Point out each leukocyte.
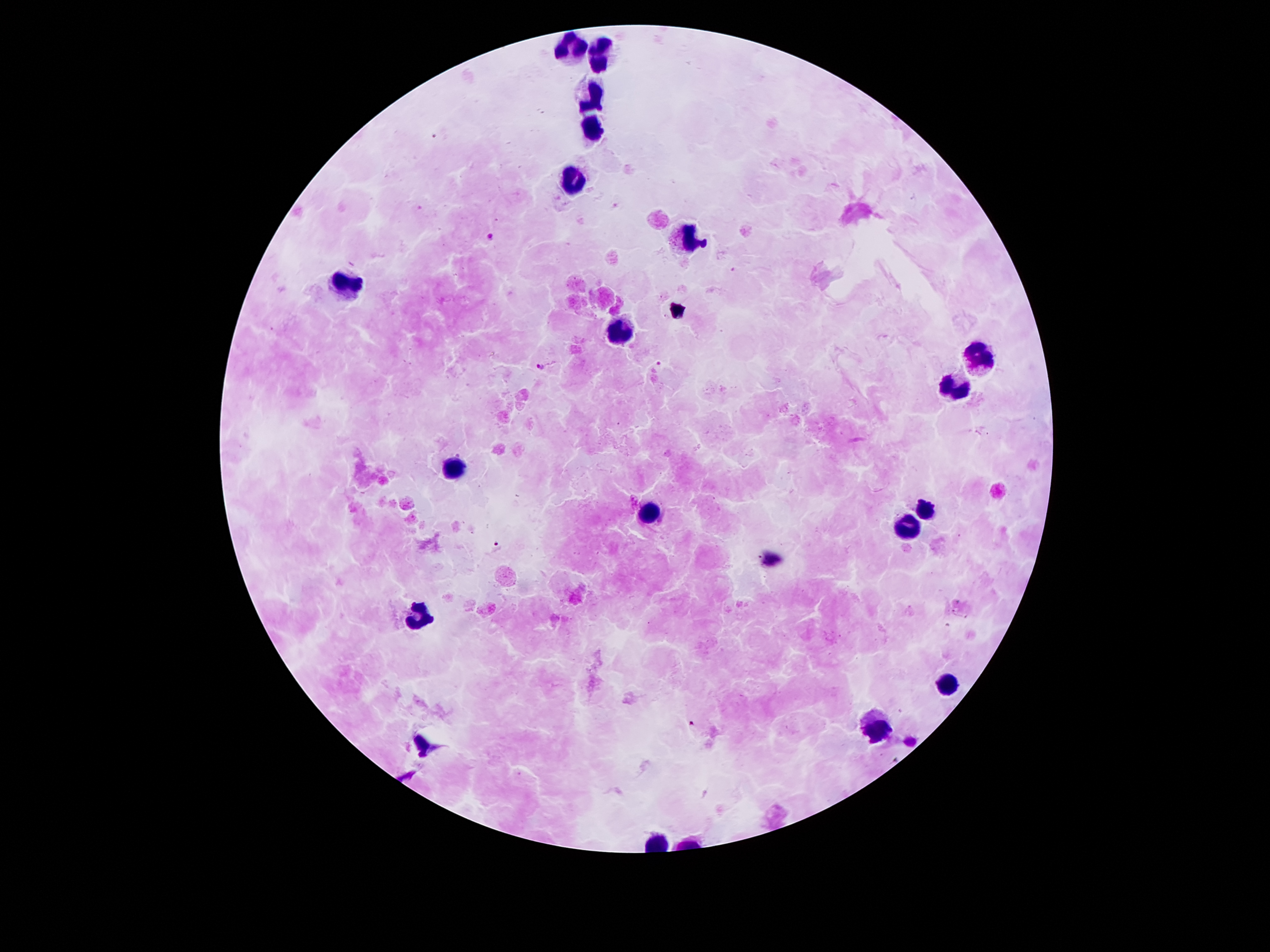

Approximate centers as (x, y) in pixels.
Leukocytes: (563, 45), (597, 57), (593, 95), (593, 131), (573, 181), (687, 239), (341, 285), (615, 332), (977, 358), (953, 385), (455, 465), (927, 505), (649, 511), (907, 527), (421, 618), (949, 682), (879, 730).

Summary:
  - Malaria parasite locations: (491, 238), (661, 364), (540, 367), (498, 545), (688, 723)
  - Magnification: 100x
  - Preparation: thick blood smear
  - Image size: 1270×952 pixels
  - Patient malaria status: infected with Plasmodium falciparum
  - Stain: Giemsa
  - Field of view: one from this slide
  - Capture: smartphone camera through the microscope eyepiece